Locate every malaria parasite.
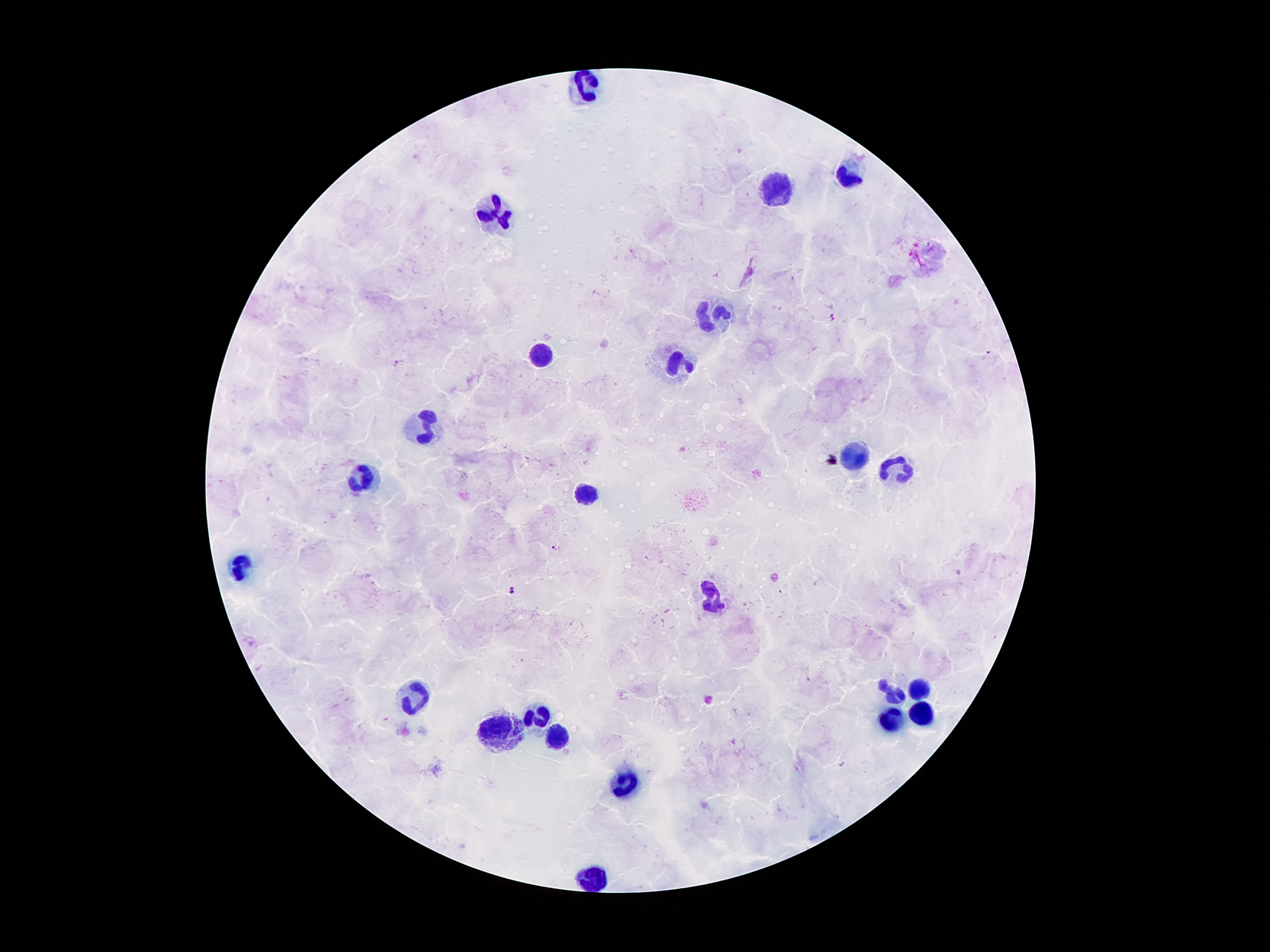

Approximate centers as (x, y) in pixels.
Malaria parasites: (990, 352), (556, 549), (512, 591).

Summary:
  - Leukocyte locations: (586, 86), (848, 176), (775, 192), (494, 216), (711, 316), (538, 353), (681, 364), (418, 427), (851, 455), (894, 469), (363, 480), (584, 493), (243, 567), (713, 598), (917, 689), (891, 693), (413, 697), (920, 712), (540, 717), (891, 722), (499, 729), (556, 737), (627, 785), (591, 879)
  - Preparation: thick peripheral-blood smear
  - Field of view: one from this slide
  - Capture: smartphone through the microscope eyepiece
  - Patient malaria status: infected with Plasmodium falciparum
  - Image size: 1270×952 pixels
  - Magnification: 100x
  - Stain: Giemsa